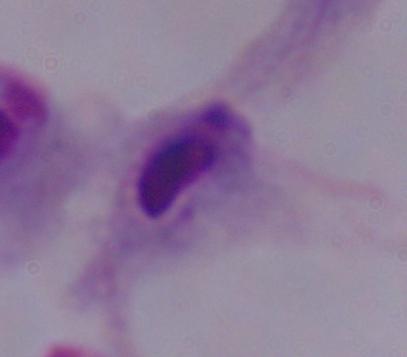
magnification = 1000x
modality = photomicrograph
identification = trichomonad